Comment on the morphology of the erythrocytes.
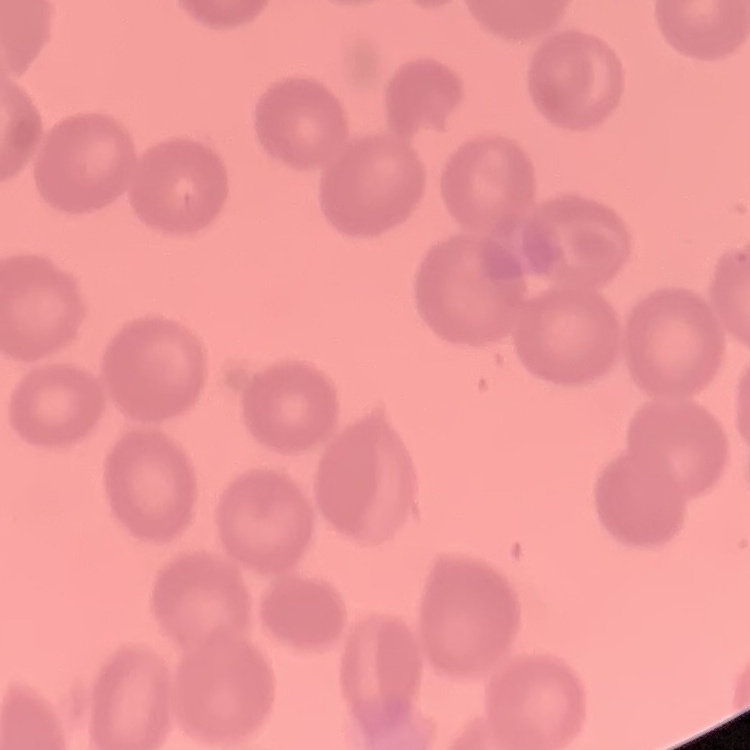

No rouleaux formation.

One tile cut from a larger photomicrograph. Thin blood smear. Field's or Giemsa stain.